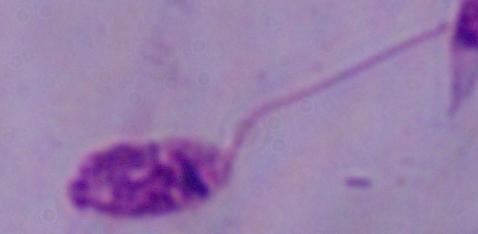

Summary:
  - Modality: photomicrograph
  - Magnification: 1000x
  - Identification: Leishmania